Assess this cell for malaria.
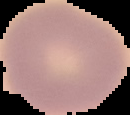
Uninfected.

Summary:
  - Image type: segmented cell region with the area outside set to black
  - Image size: 130×115 pixels
  - Preparation: thin blood film